Locate every white blood cell.
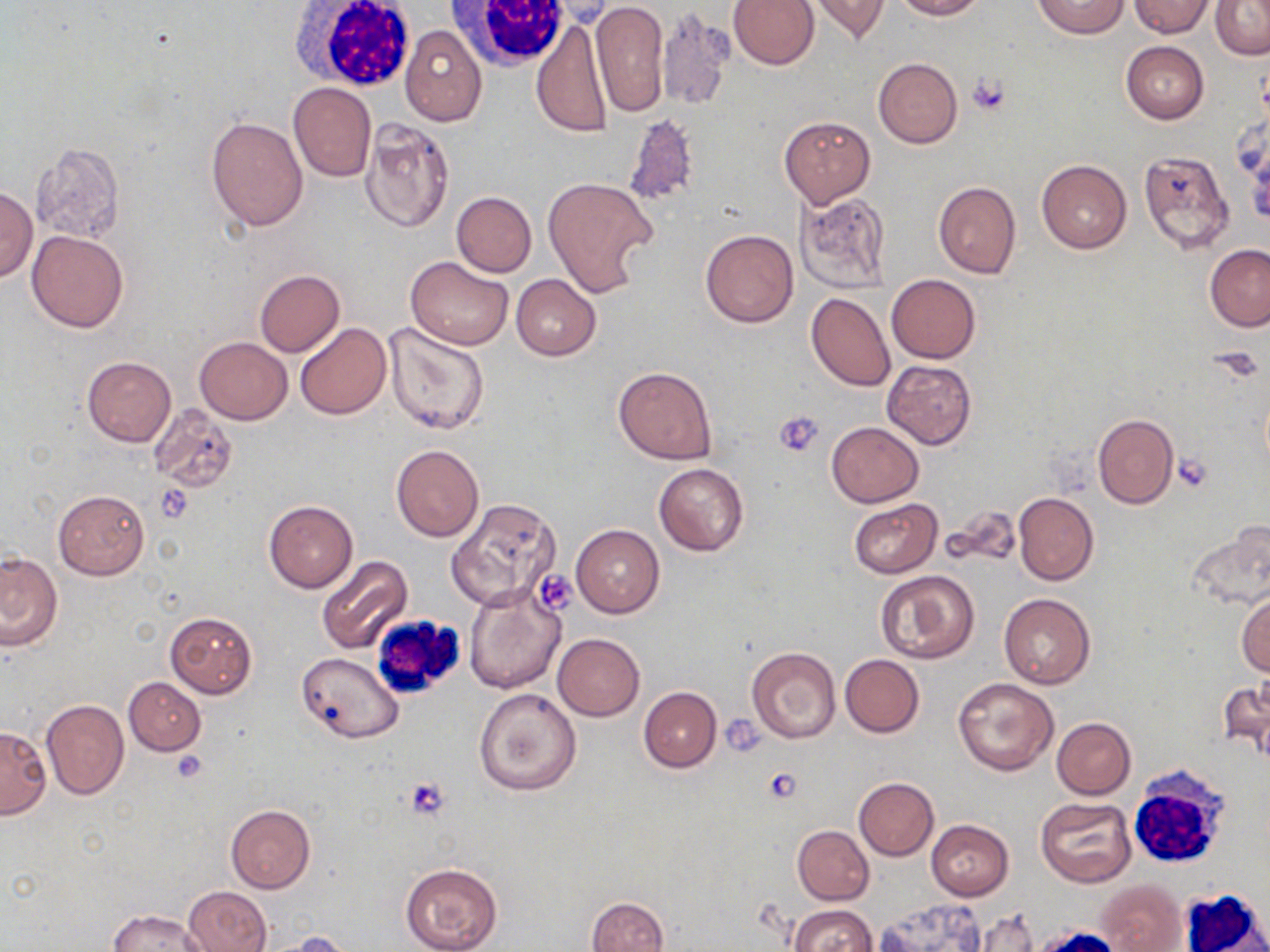

Approximate bounding boxes as (x1, y1, x2, y2) in pixels.
White blood cells: (290, 0, 420, 93), (449, 0, 573, 73), (368, 613, 468, 702), (1132, 764, 1229, 868), (1179, 887, 1268, 952).

slide-level diagnosis = negative for blood parasites
platelet locations = approximate bounding boxes as (x1, y1, x2, y2) in pixels: (968, 73, 1009, 113), (774, 411, 824, 458), (1173, 454, 1212, 492), (156, 484, 193, 523), (723, 717, 766, 756), (170, 750, 207, 782), (764, 767, 802, 802), (405, 777, 452, 821)
field of view = one of a larger specimen
image size = 1270×952 pixels
uninfected red blood cell locations = approximate bounding boxes as (x1, y1, x2, y2) in pixels: (729, 0, 818, 69), (805, 0, 891, 44), (894, 0, 985, 20), (1132, 0, 1213, 38), (1210, 0, 1270, 59), (537, 1, 618, 27), (591, 1, 669, 116), (1033, 1, 1128, 38), (656, 6, 735, 113), (532, 18, 613, 139), (400, 26, 487, 126), (1121, 40, 1208, 123), (873, 57, 963, 148), (289, 82, 376, 181), (779, 115, 875, 207), (206, 116, 308, 231), (624, 116, 700, 211), (360, 119, 455, 233), (31, 142, 125, 241), (1137, 148, 1235, 254), (1037, 159, 1131, 253), (542, 176, 658, 297), (932, 180, 1021, 279), (0, 187, 37, 281), (794, 190, 892, 294), (452, 192, 537, 277), (431, 198, 528, 347), (26, 230, 129, 333), (700, 230, 798, 329), (1205, 243, 1270, 332), (406, 256, 514, 351), (253, 270, 345, 357), (887, 273, 981, 363), (511, 274, 601, 359), (805, 292, 896, 392), (295, 323, 391, 420), (383, 323, 490, 434), (194, 338, 291, 424), (82, 355, 176, 446), (883, 360, 977, 448), (613, 366, 718, 465), (151, 404, 237, 494), (1092, 413, 1179, 510), (826, 422, 924, 508), (391, 444, 484, 543), (653, 462, 748, 557), (53, 489, 149, 580), (1013, 493, 1098, 586), (263, 498, 359, 593), (447, 498, 561, 611), (849, 498, 942, 577), (944, 505, 1021, 568), (1185, 523, 1270, 612), (571, 525, 664, 617), (0, 551, 62, 650), (316, 555, 413, 653), (877, 570, 980, 663), (463, 585, 565, 695), (999, 593, 1095, 689), (1237, 593, 1270, 676), (164, 612, 257, 699), (552, 633, 645, 721), (747, 647, 841, 743), (297, 652, 404, 742), (840, 654, 925, 737), (953, 676, 1058, 776), (124, 677, 205, 754), (1218, 677, 1270, 762), (639, 687, 721, 772), (474, 688, 582, 795), (41, 699, 129, 801), (1052, 717, 1136, 799), (0, 725, 51, 818), (853, 777, 939, 859), (1036, 798, 1136, 887), (225, 805, 316, 893), (926, 820, 1013, 900), (792, 825, 874, 904), (401, 863, 503, 952), (1095, 879, 1187, 952), (183, 886, 270, 952), (587, 896, 669, 952), (875, 898, 989, 951), (788, 904, 878, 951), (109, 910, 208, 951), (971, 912, 1038, 952), (271, 931, 354, 952)
modality = optical microscopy
preparation = thin blood film
magnification = 1000x
stain = May-Grünwald-Giemsa